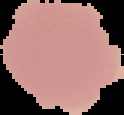

Malaria status: uninfected. From a thin blood film. Image is 124×115 pixels. Segmented cell region on a black background.